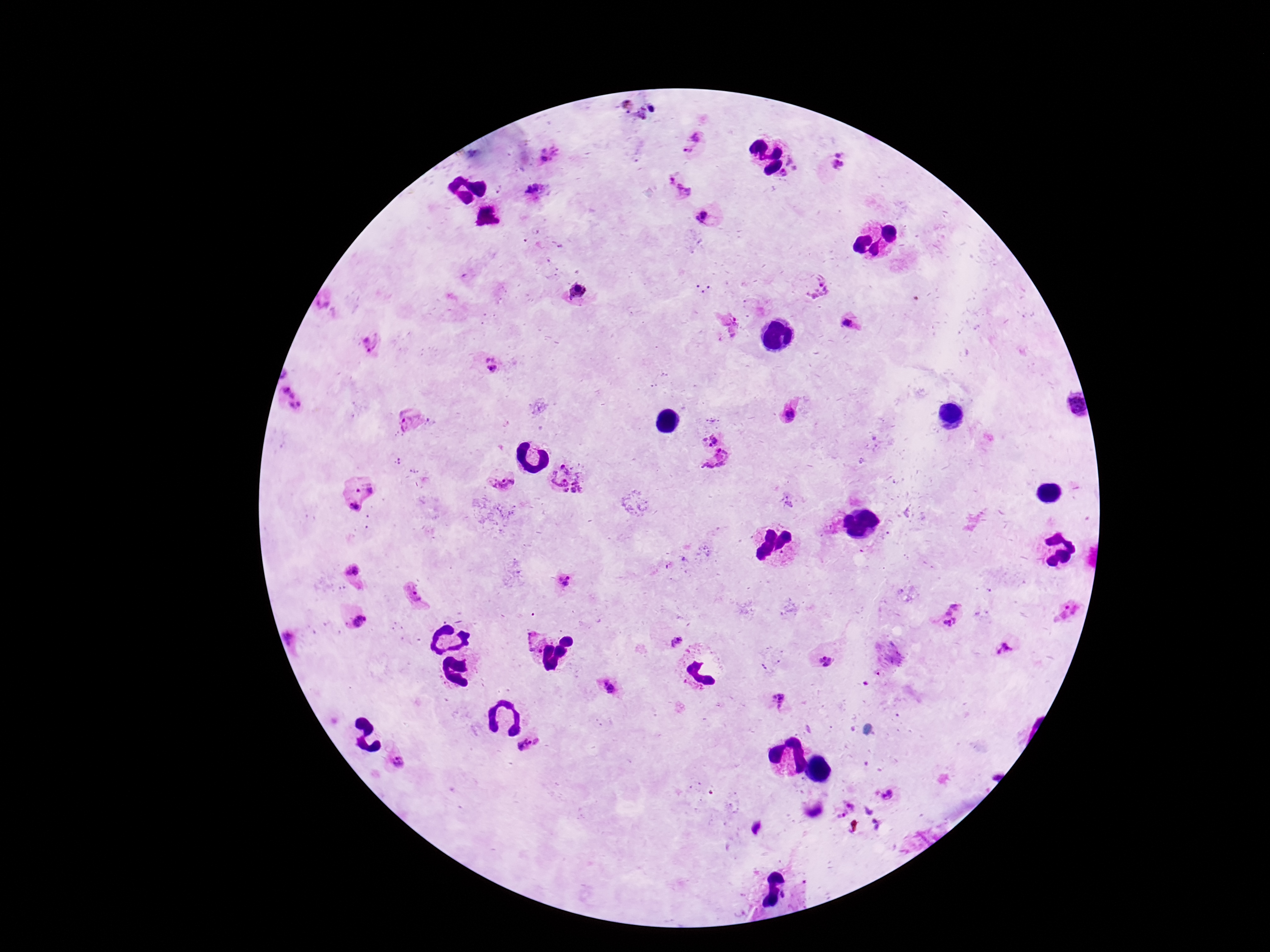 Approximate object centers, in pixels from the top-left corner. Plasmodium parasite locations: (x=693, y=144), (x=551, y=154), (x=839, y=162), (x=679, y=186), (x=535, y=193), (x=703, y=217), (x=818, y=286), (x=322, y=303), (x=850, y=324), (x=728, y=326), (x=370, y=343), (x=488, y=364), (x=288, y=398), (x=1072, y=404), (x=789, y=412), (x=411, y=422), (x=708, y=435), (x=720, y=466), (x=564, y=479), (x=501, y=480), (x=354, y=493), (x=352, y=574), (x=567, y=582), (x=417, y=595), (x=1067, y=611), (x=952, y=613), (x=354, y=615), (x=290, y=635), (x=673, y=640), (x=530, y=641), (x=1005, y=648), (x=823, y=663), (x=607, y=686), (x=780, y=702), (x=530, y=745), (x=395, y=762), (x=889, y=796), (x=844, y=808). 100x magnification. Single field of view. Image is 1270×952 pixels. Thick peripheral-blood smear. Patient malaria status: positive. Giemsa-stained preparation. Smartphone photograph taken through the microscope eyepiece.